Identify the parasite.
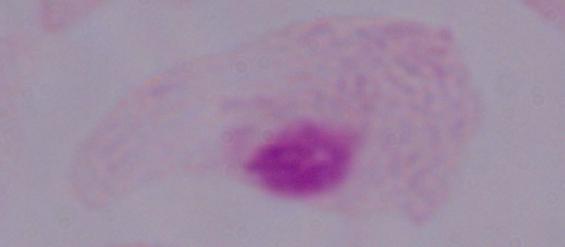
This is a trichomonad.

modality = photomicrograph
magnification = 1000x